Name the blood parasite species.
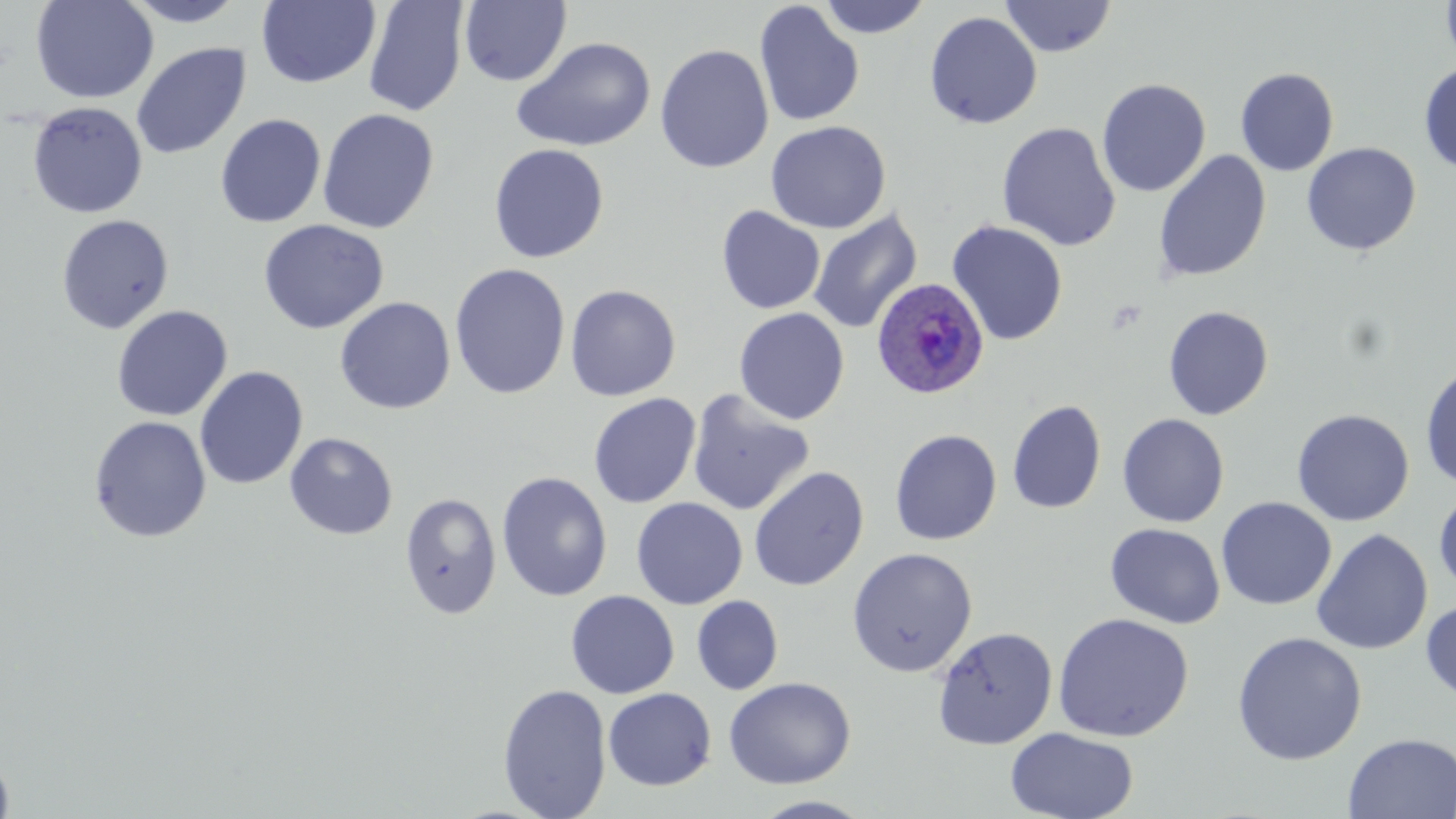

Plasmodium ovale.

Approximate bounding boxes as (x1,y1)-(x2,y2) corner pairs in pixels. Plasmodium ovale-infected red blood cell locations: (872,277)-(989,399). Platelet locations: (1105,298)-(1149,334). Uninfected red blood cell locations: (31,0)-(158,105), (119,0)-(250,26), (817,0)-(932,39), (1000,0)-(1117,58), (1440,0)-(1456,70), (256,1)-(381,88), (363,1)-(469,117), (459,1)-(571,86), (753,2)-(865,127), (924,11)-(1043,129), (511,36)-(657,153), (131,43)-(251,160), (654,43)-(774,173), (1418,62)-(1456,175), (1235,67)-(1340,176), (1096,78)-(1211,197), (27,101)-(147,219), (317,108)-(440,233), (215,114)-(326,228), (765,120)-(891,234), (997,122)-(1121,252), (1301,142)-(1421,256), (488,143)-(610,263), (1153,150)-(1272,283), (715,205)-(825,314), (808,210)-(923,334), (56,214)-(174,334), (257,219)-(390,334), (947,220)-(1068,346), (449,263)-(571,400), (565,284)-(681,401), (335,297)-(456,414), (111,305)-(233,422), (1162,305)-(1274,420), (734,308)-(850,425), (1420,362)-(1456,491), (194,366)-(308,490), (686,390)-(816,517), (588,393)-(702,508), (1007,399)-(1107,514), (1291,408)-(1415,526), (1116,413)-(1229,527), (88,416)-(212,543), (889,429)-(1002,545), (284,432)-(398,540), (749,466)-(869,592), (496,471)-(613,602), (1434,488)-(1456,595), (399,492)-(502,619), (631,497)-(748,610), (1216,497)-(1336,610), (1105,523)-(1225,629), (1311,529)-(1433,655), (846,547)-(977,677), (566,590)-(680,699), (692,595)-(783,695), (1420,597)-(1456,705), (1053,612)-(1194,742), (932,626)-(1057,749), (1231,631)-(1367,765), (723,677)-(856,789), (497,683)-(612,819), (603,687)-(717,790), (1006,726)-(1139,819), (1343,732)-(1456,819), (0,746)-(15,818), (751,795)-(876,818). Thin blood smear. Single field of view. Captured at 1000x magnification. Image is 1456×819 pixels. May-Grünwald-Giemsa-stained preparation. Optical microscopy.